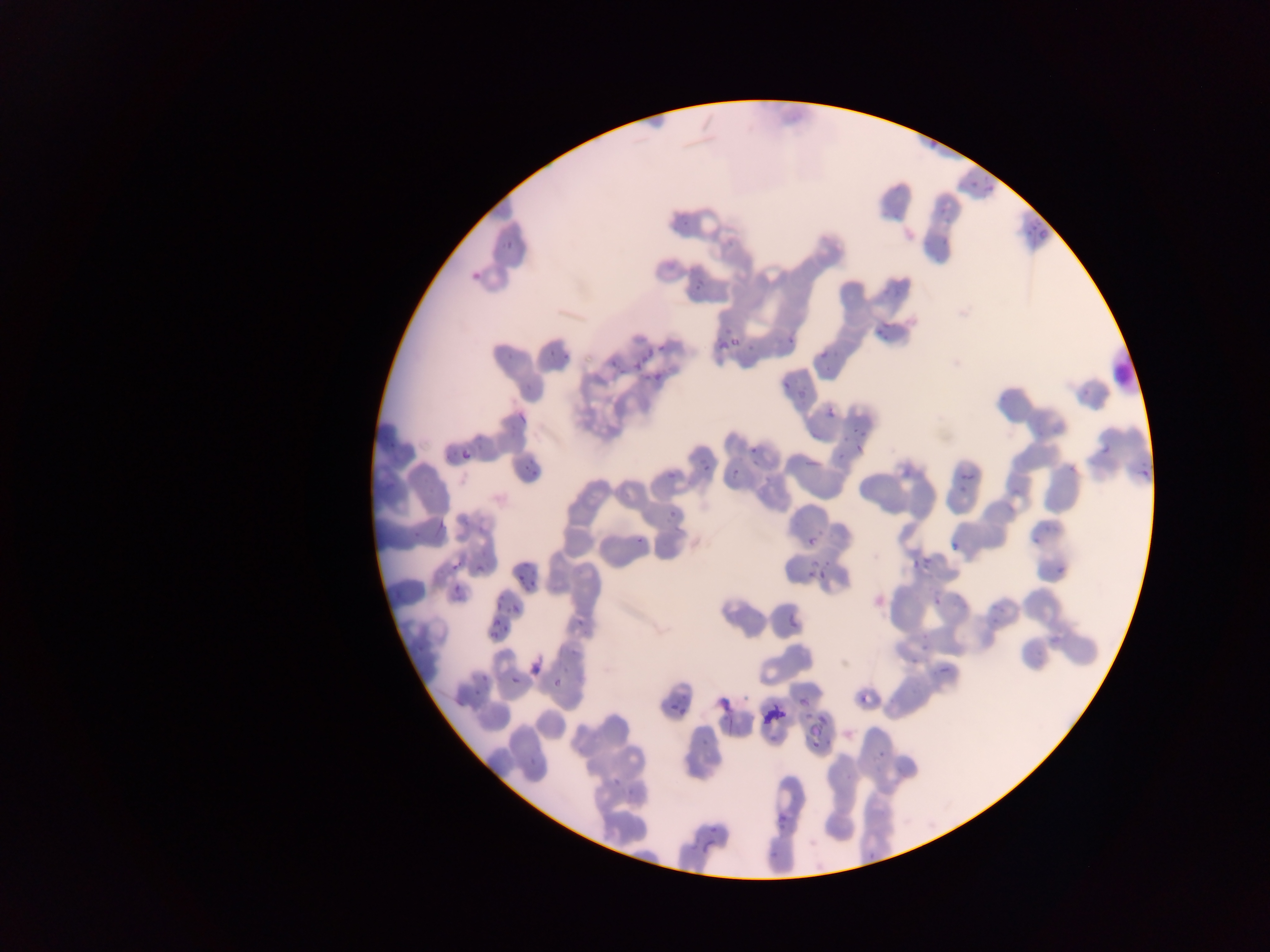

Approximate bounding boxes as (left, top, right, bottom) in pixels.
Summary:
  - Malaria parasite locations: (470, 268, 486, 286), (696, 279, 706, 294), (781, 330, 798, 346), (709, 332, 731, 353), (726, 336, 745, 352), (649, 341, 670, 351), (499, 346, 515, 362), (544, 347, 558, 364), (630, 350, 650, 372), (560, 353, 571, 362), (610, 361, 622, 379), (642, 370, 665, 387), (780, 372, 796, 393), (517, 398, 538, 425), (824, 404, 839, 421), (750, 436, 765, 453), (850, 439, 866, 455), (1093, 440, 1114, 459), (460, 441, 475, 461), (698, 456, 712, 470), (804, 456, 821, 472), (519, 457, 540, 479), (1067, 458, 1084, 473), (727, 463, 742, 482), (1137, 463, 1157, 476), (899, 465, 912, 482), (952, 471, 978, 496), (669, 505, 682, 517), (431, 509, 448, 536), (1030, 525, 1052, 542), (632, 533, 642, 545), (804, 535, 815, 546), (947, 537, 958, 553), (907, 547, 936, 569), (447, 557, 458, 574), (807, 562, 827, 580), (1057, 562, 1070, 574), (514, 564, 528, 583), (473, 565, 486, 576), (447, 579, 465, 602), (524, 582, 542, 594), (989, 592, 1009, 624), (932, 596, 945, 604), (510, 603, 523, 616), (782, 611, 802, 636), (486, 613, 497, 628), (575, 616, 582, 629), (497, 623, 509, 639), (1045, 635, 1057, 649), (920, 640, 932, 651), (933, 661, 958, 672), (531, 664, 542, 675), (467, 671, 492, 698), (554, 672, 564, 691), (509, 674, 523, 689), (860, 686, 877, 707), (796, 691, 816, 706), (670, 701, 680, 711), (807, 715, 830, 740), (696, 729, 714, 749), (612, 774, 628, 792), (776, 808, 790, 825), (702, 823, 719, 855)
  - Country: Ghana
  - Preparation: thin blood smear
  - Capture: mobile-phone photograph through a microscope
  - Image size: 1270×952 pixels
  - Field of view: single